Outline each Plasmodium vivax-infected red blood cell.
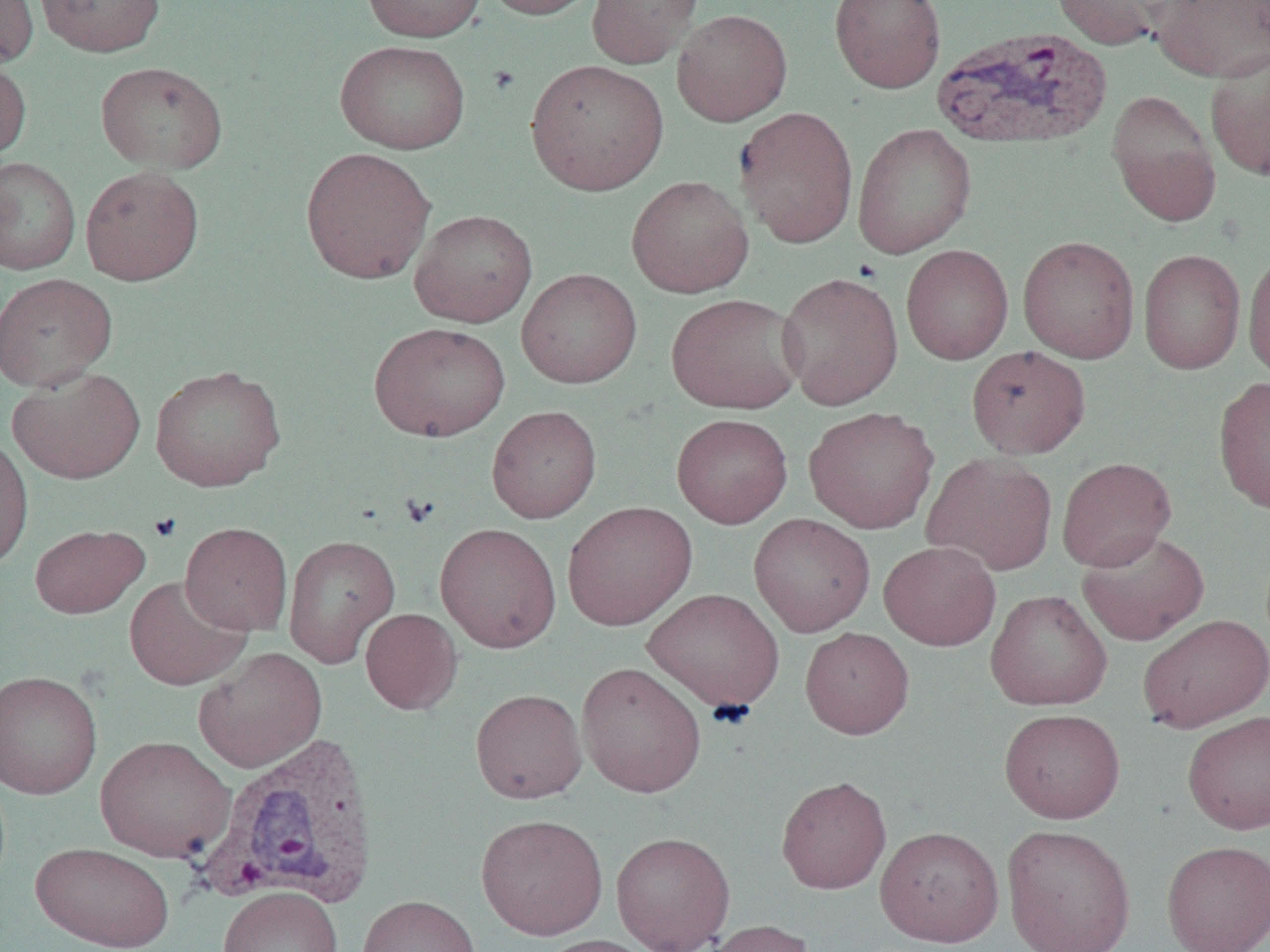
Approximate bounding boxes as (x1,y1)-(x2,y2) corner pairs in pixels.
Plasmodium vivax-infected red blood cells: (929,26)-(1113,152), (196,731)-(382,911).

Summary:
  - Uninfected red blood cell locations: (0,0)-(38,68), (34,0)-(165,57), (361,0)-(487,42), (480,0)-(604,20), (586,0)-(704,69), (829,0)-(946,94), (1051,0)-(1180,50), (1149,0)-(1270,82), (672,9)-(793,126), (335,39)-(471,155), (1204,49)-(1270,182), (0,55)-(31,164), (525,59)-(669,195), (96,61)-(228,173), (1106,89)-(1221,228), (734,105)-(859,248), (852,123)-(976,258), (300,147)-(436,284), (0,157)-(80,275), (80,166)-(204,286), (626,175)-(754,298), (408,209)-(537,328), (1017,235)-(1140,363), (901,244)-(1013,365), (1138,249)-(1246,374), (1243,251)-(1270,381), (516,268)-(642,388), (777,271)-(903,410), (0,272)-(117,392), (665,292)-(805,414), (369,322)-(511,442), (966,345)-(1090,458), (150,364)-(286,492), (7,367)-(145,484), (1212,375)-(1270,516), (486,405)-(602,523), (803,406)-(940,534), (671,413)-(793,528), (0,433)-(34,573), (922,452)-(1058,576), (1056,456)-(1176,572), (562,501)-(697,631), (748,513)-(875,637), (179,521)-(293,636), (435,523)-(561,653), (29,524)-(148,618), (1076,529)-(1210,645), (283,534)-(401,668), (879,540)-(1001,650), (124,575)-(251,691), (642,588)-(784,712), (985,589)-(1112,711), (360,608)-(462,715), (1138,614)-(1270,732), (800,627)-(914,739), (193,646)-(327,773), (576,662)-(707,798), (0,670)-(103,799), (470,688)-(587,803), (999,708)-(1125,823), (1182,710)-(1270,835), (95,735)-(235,862), (776,775)-(891,894), (476,813)-(608,940), (1001,824)-(1136,952), (875,825)-(1004,946), (611,831)-(735,952), (1161,839)-(1270,952), (31,841)-(175,951), (218,886)-(343,952), (356,894)-(481,952), (700,919)-(816,952), (536,934)-(660,952)
  - Platelet locations: (400,492)-(439,527), (148,512)-(182,543)
  - Slide-level diagnosis: Plasmodium vivax
  - Field of view: single
  - Image size: 1270×952 pixels
  - Modality: optical microscopy
  - Preparation: thin blood smear
  - Magnification: 1000x